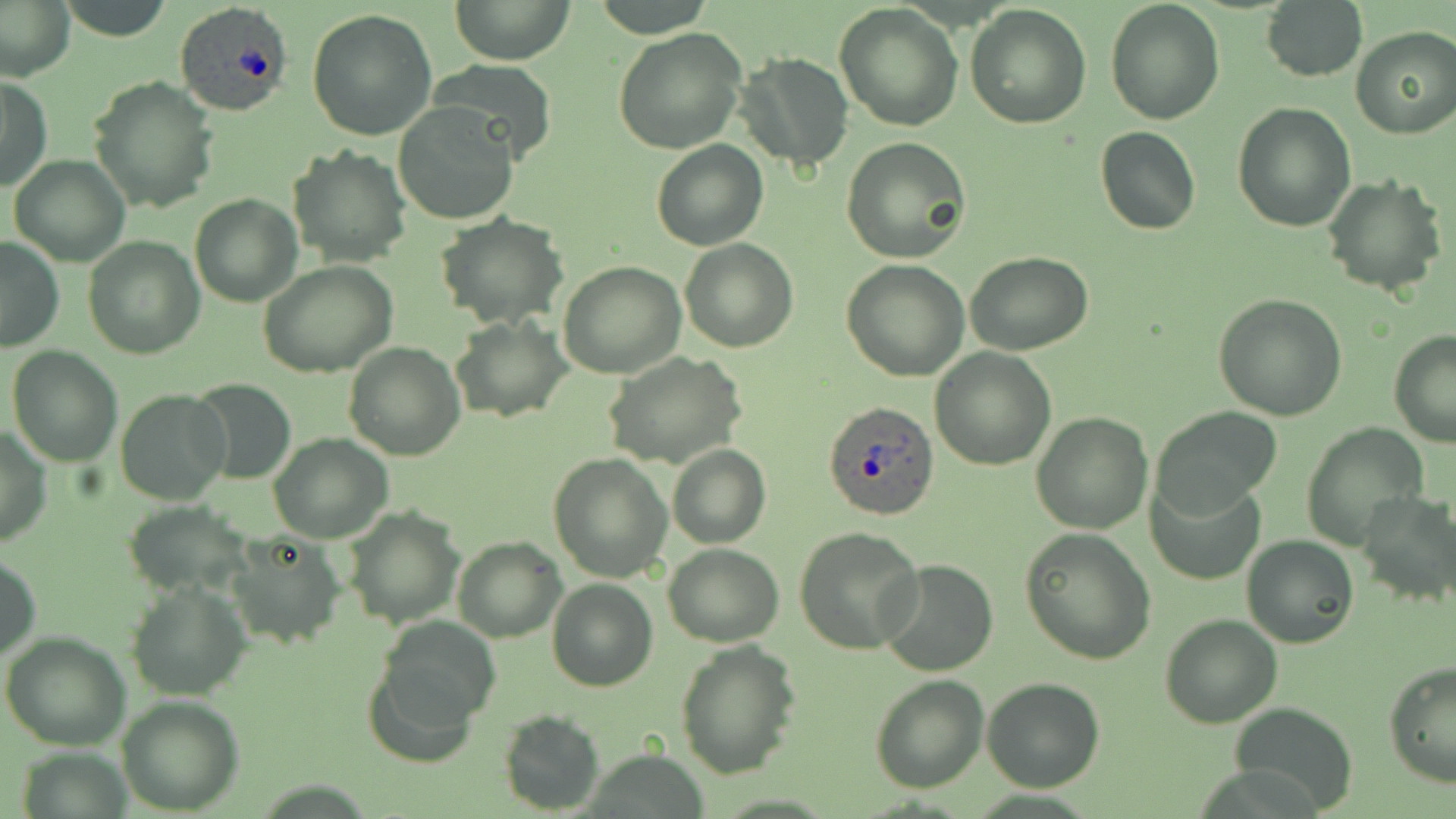

slide-level diagnosis = Plasmodium ovale
image size = 1456×819 pixels
modality = optical microscopy
magnification = 1000x
Plasmodium ovale-infected red blood cell locations = approximate bounding boxes as named x1/y1/x2/y2 corners in pixels: (x1=174, y1=1, x2=294, y2=116), (x1=823, y1=402, x2=941, y2=520)
uninfected red blood cell locations = approximate bounding boxes as named x1/y1/x2/y2 corners in pixels: (x1=450, y1=0, x2=574, y2=65), (x1=1261, y1=0, x2=1367, y2=84), (x1=0, y1=1, x2=74, y2=80), (x1=56, y1=1, x2=176, y2=41), (x1=1103, y1=1, x2=1226, y2=125), (x1=833, y1=4, x2=964, y2=133), (x1=965, y1=5, x2=1092, y2=129), (x1=307, y1=9, x2=439, y2=141), (x1=1349, y1=26, x2=1456, y2=139), (x1=613, y1=28, x2=748, y2=154), (x1=734, y1=52, x2=853, y2=172), (x1=430, y1=60, x2=557, y2=163), (x1=89, y1=75, x2=219, y2=213), (x1=2, y1=76, x2=52, y2=192), (x1=393, y1=101, x2=523, y2=226), (x1=1233, y1=101, x2=1358, y2=230), (x1=1095, y1=126, x2=1201, y2=234), (x1=840, y1=137, x2=972, y2=264), (x1=651, y1=139, x2=769, y2=251), (x1=287, y1=144, x2=413, y2=267), (x1=8, y1=156, x2=131, y2=267), (x1=1323, y1=176, x2=1447, y2=296), (x1=190, y1=194, x2=302, y2=307), (x1=434, y1=214, x2=569, y2=329), (x1=82, y1=235, x2=205, y2=358), (x1=0, y1=237, x2=64, y2=352), (x1=679, y1=239, x2=798, y2=353), (x1=966, y1=252, x2=1094, y2=356), (x1=257, y1=260, x2=399, y2=378), (x1=841, y1=260, x2=970, y2=382), (x1=556, y1=261, x2=686, y2=379), (x1=1213, y1=294, x2=1348, y2=422), (x1=450, y1=316, x2=571, y2=422), (x1=1388, y1=327, x2=1456, y2=448), (x1=343, y1=342, x2=466, y2=460), (x1=8, y1=345, x2=123, y2=467), (x1=929, y1=347, x2=1056, y2=470), (x1=602, y1=350, x2=747, y2=469), (x1=188, y1=379, x2=296, y2=485), (x1=117, y1=390, x2=232, y2=506), (x1=1153, y1=406, x2=1282, y2=516), (x1=1030, y1=413, x2=1153, y2=533), (x1=1303, y1=423, x2=1427, y2=552), (x1=0, y1=426, x2=50, y2=547), (x1=269, y1=434, x2=392, y2=544), (x1=666, y1=444, x2=771, y2=548), (x1=548, y1=452, x2=673, y2=583), (x1=1148, y1=473, x2=1264, y2=585), (x1=1357, y1=489, x2=1455, y2=606), (x1=122, y1=502, x2=257, y2=599), (x1=343, y1=507, x2=464, y2=627), (x1=793, y1=526, x2=925, y2=655), (x1=1019, y1=528, x2=1155, y2=666), (x1=225, y1=532, x2=345, y2=650), (x1=451, y1=535, x2=566, y2=641), (x1=1240, y1=535, x2=1360, y2=648), (x1=662, y1=542, x2=785, y2=647), (x1=1, y1=553, x2=40, y2=665), (x1=875, y1=558, x2=1000, y2=677), (x1=547, y1=578, x2=659, y2=692), (x1=126, y1=580, x2=252, y2=701), (x1=1160, y1=614, x2=1283, y2=729), (x1=367, y1=623, x2=496, y2=761), (x1=2, y1=634, x2=130, y2=750), (x1=675, y1=640, x2=801, y2=778), (x1=1384, y1=658, x2=1456, y2=787), (x1=869, y1=673, x2=991, y2=793), (x1=981, y1=677, x2=1105, y2=792), (x1=116, y1=695, x2=245, y2=815), (x1=1232, y1=703, x2=1357, y2=812), (x1=499, y1=709, x2=605, y2=815), (x1=18, y1=746, x2=132, y2=819)
preparation = thin blood smear
field of view = single
stain = May-Grünwald-Giemsa